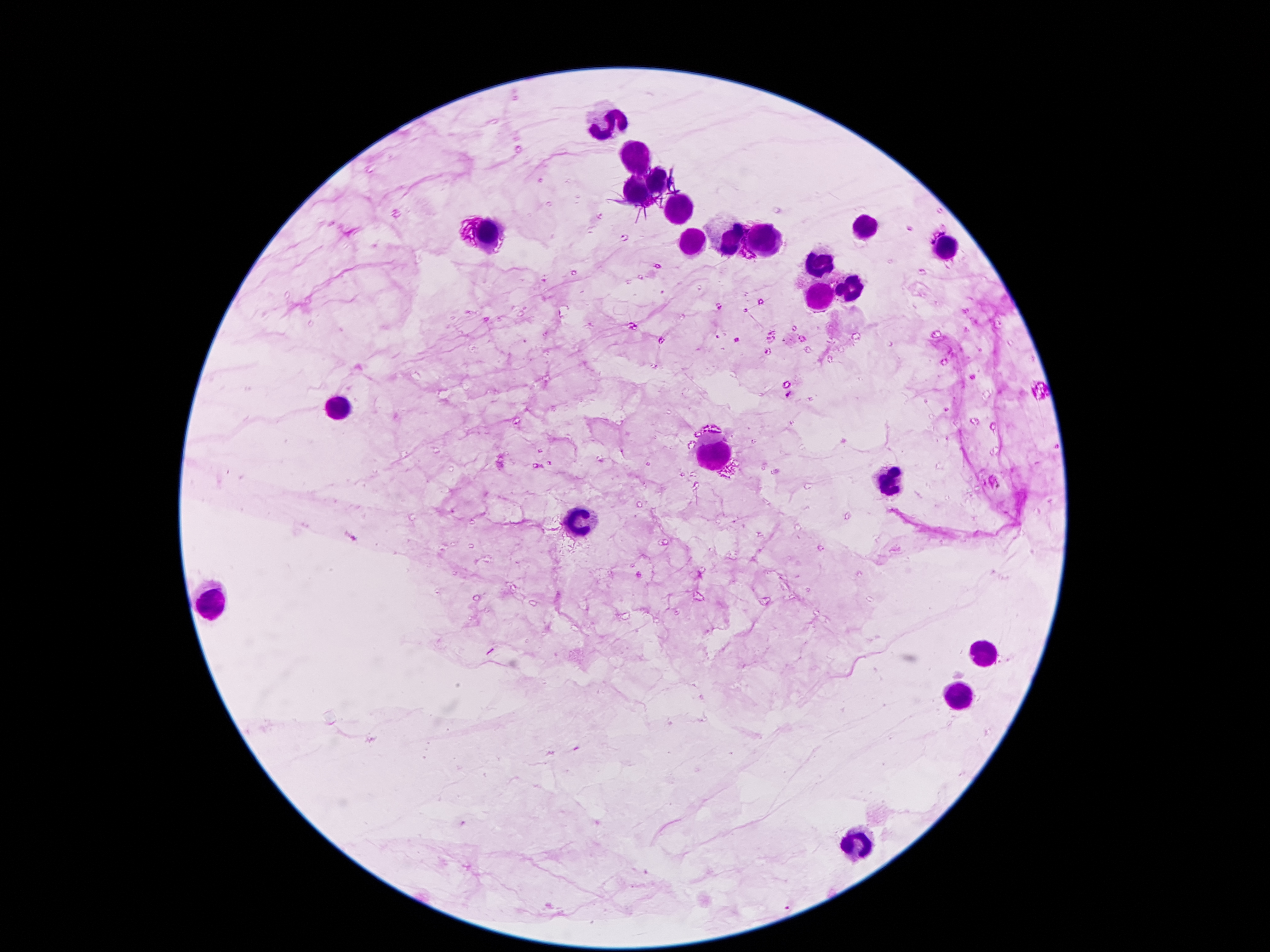

Approximate object centers, in pixels from the top-left corner. Malaria parasite locations: (x=737, y=340), (x=788, y=395). Leukocyte locations: (x=609, y=121), (x=637, y=159), (x=659, y=179), (x=639, y=193), (x=683, y=213), (x=865, y=229), (x=487, y=235), (x=733, y=239), (x=769, y=243), (x=693, y=245), (x=949, y=249), (x=819, y=261), (x=849, y=291), (x=819, y=297), (x=337, y=409), (x=715, y=451), (x=891, y=479), (x=575, y=522), (x=207, y=604), (x=985, y=654), (x=963, y=698), (x=855, y=846). 100x magnification. Thick peripheral-blood smear. One field from this slide. Patient malaria status: positive for Plasmodium falciparum. Photographed through the microscope eyepiece with a smartphone camera. Image is 1270×952 pixels. Giemsa stain.